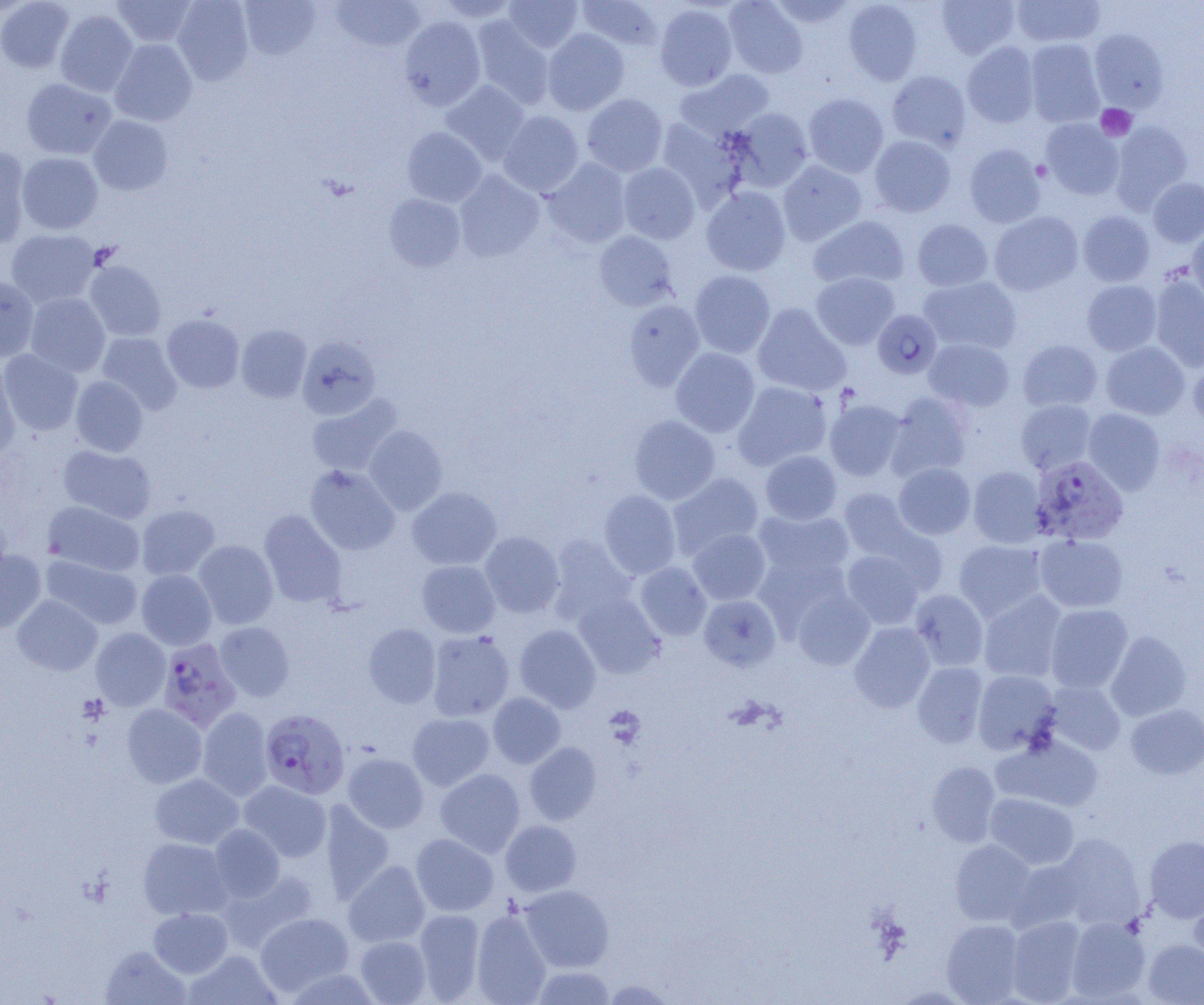

slide-level diagnosis = Plasmodium falciparum
modality = optical microscopy
magnification = 1000x
uninfected red blood cell locations = approximate bounding boxes as (x1, y1, x2, y2) in pixels: (0, 0, 74, 73), (111, 0, 197, 48), (172, 0, 254, 84), (330, 0, 426, 52), (434, 0, 520, 23), (503, 0, 583, 53), (577, 0, 664, 51), (724, 0, 808, 78), (768, 0, 856, 29), (843, 0, 922, 85), (936, 0, 1020, 58), (1011, 0, 1106, 48), (239, 1, 320, 60), (654, 4, 737, 91), (55, 9, 138, 97), (399, 16, 485, 110), (470, 17, 554, 109), (542, 29, 629, 115), (1089, 30, 1169, 112), (1024, 38, 1105, 127), (110, 39, 197, 126), (962, 42, 1040, 127), (675, 69, 774, 140), (887, 70, 971, 150), (21, 79, 116, 160), (441, 80, 530, 164), (581, 93, 668, 177), (803, 93, 889, 177), (727, 108, 813, 192), (498, 110, 584, 196), (88, 115, 172, 196), (656, 118, 747, 208), (1040, 119, 1124, 200), (1110, 120, 1193, 212), (403, 127, 486, 207), (869, 135, 956, 217), (964, 143, 1045, 227), (0, 146, 30, 247), (17, 152, 103, 234), (543, 158, 631, 248), (777, 161, 867, 246), (618, 162, 700, 244), (454, 171, 544, 261), (1147, 178, 1204, 247), (701, 186, 791, 276), (384, 193, 466, 272), (988, 211, 1083, 295), (1078, 211, 1155, 287), (808, 215, 910, 290), (912, 219, 993, 291), (1187, 226, 1204, 304), (6, 229, 100, 308), (594, 230, 679, 311), (84, 261, 166, 341), (689, 270, 775, 358), (811, 272, 899, 349), (0, 276, 39, 361), (919, 276, 1021, 354), (1149, 276, 1204, 371), (1082, 280, 1161, 355), (25, 293, 110, 377), (623, 299, 705, 392), (752, 303, 850, 396), (873, 310, 942, 379), (162, 314, 244, 393), (236, 325, 311, 402), (97, 332, 182, 414), (297, 336, 381, 420), (924, 338, 1015, 412), (1017, 339, 1102, 412), (1101, 342, 1189, 420), (670, 347, 760, 437), (0, 349, 83, 436), (1188, 354, 1204, 432), (0, 363, 20, 459), (70, 376, 148, 456), (732, 381, 832, 470), (885, 391, 973, 480), (306, 394, 401, 477), (825, 399, 906, 481), (1016, 399, 1097, 474), (1083, 408, 1165, 494), (629, 415, 720, 505), (363, 424, 447, 516), (58, 444, 156, 523), (760, 450, 841, 525), (894, 463, 975, 539), (305, 465, 400, 555), (968, 466, 1047, 548), (668, 472, 763, 559), (407, 486, 502, 570), (599, 489, 681, 579), (839, 489, 918, 562), (42, 501, 144, 576), (136, 504, 220, 580), (753, 508, 854, 584), (259, 510, 346, 607), (0, 513, 11, 589), (688, 528, 771, 604), (480, 532, 564, 617), (1034, 534, 1128, 612), (548, 535, 636, 623), (193, 540, 278, 629), (954, 540, 1047, 622), (0, 550, 46, 633), (841, 550, 924, 628), (41, 555, 143, 630), (416, 560, 500, 638), (636, 562, 711, 641), (136, 569, 216, 650), (792, 589, 874, 670), (910, 589, 988, 671), (978, 591, 1066, 682), (574, 593, 663, 678), (12, 595, 102, 675), (698, 595, 780, 671), (1046, 604, 1132, 693), (215, 622, 294, 701), (849, 622, 935, 712), (363, 623, 441, 708), (515, 624, 600, 712), (91, 628, 170, 711), (427, 630, 515, 721), (1106, 630, 1191, 721), (912, 662, 988, 748), (973, 670, 1060, 754), (1045, 681, 1125, 755), (487, 692, 566, 768), (1126, 703, 1204, 779), (122, 704, 207, 788), (198, 707, 273, 800), (408, 712, 495, 791), (993, 734, 1102, 812), (525, 742, 601, 825), (343, 752, 429, 833), (927, 762, 1000, 847), (435, 768, 525, 857), (150, 774, 243, 849), (240, 781, 331, 862), (985, 793, 1079, 870), (318, 801, 395, 904), (500, 820, 582, 896), (209, 824, 284, 902), (410, 833, 499, 916), (1055, 834, 1144, 927), (1145, 835, 1204, 922), (138, 837, 232, 920), (949, 840, 1036, 926), (1008, 858, 1087, 932), (343, 860, 430, 947), (219, 869, 319, 951), (519, 884, 614, 972), (1188, 889, 1204, 970), (148, 907, 233, 977), (414, 908, 485, 1002), (470, 909, 552, 1005), (255, 912, 353, 995), (1006, 916, 1086, 1004), (1066, 917, 1150, 1002), (941, 919, 1025, 1004), (355, 936, 431, 1004), (1143, 939, 1204, 1005), (101, 945, 189, 1004), (185, 950, 280, 1005), (531, 966, 616, 1004), (283, 967, 383, 1005), (602, 979, 677, 1004)
Plasmodium falciparum-infected red blood cell locations = approximate bounding boxes as (x1, y1, x2, y2) in pixels: (1029, 458, 1126, 552), (157, 638, 241, 732), (260, 708, 350, 800)
preparation = thin blood film
platelet locations = approximate bounding boxes as (x1, y1, x2, y2) in pixels: (1096, 104, 1137, 141), (605, 706, 646, 748)
image size = 1204×1005 pixels
field of view = single